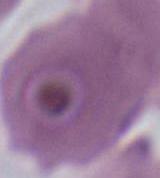

modality: photomicrograph
identification: Plasmodium
magnification: 400x or 1000x